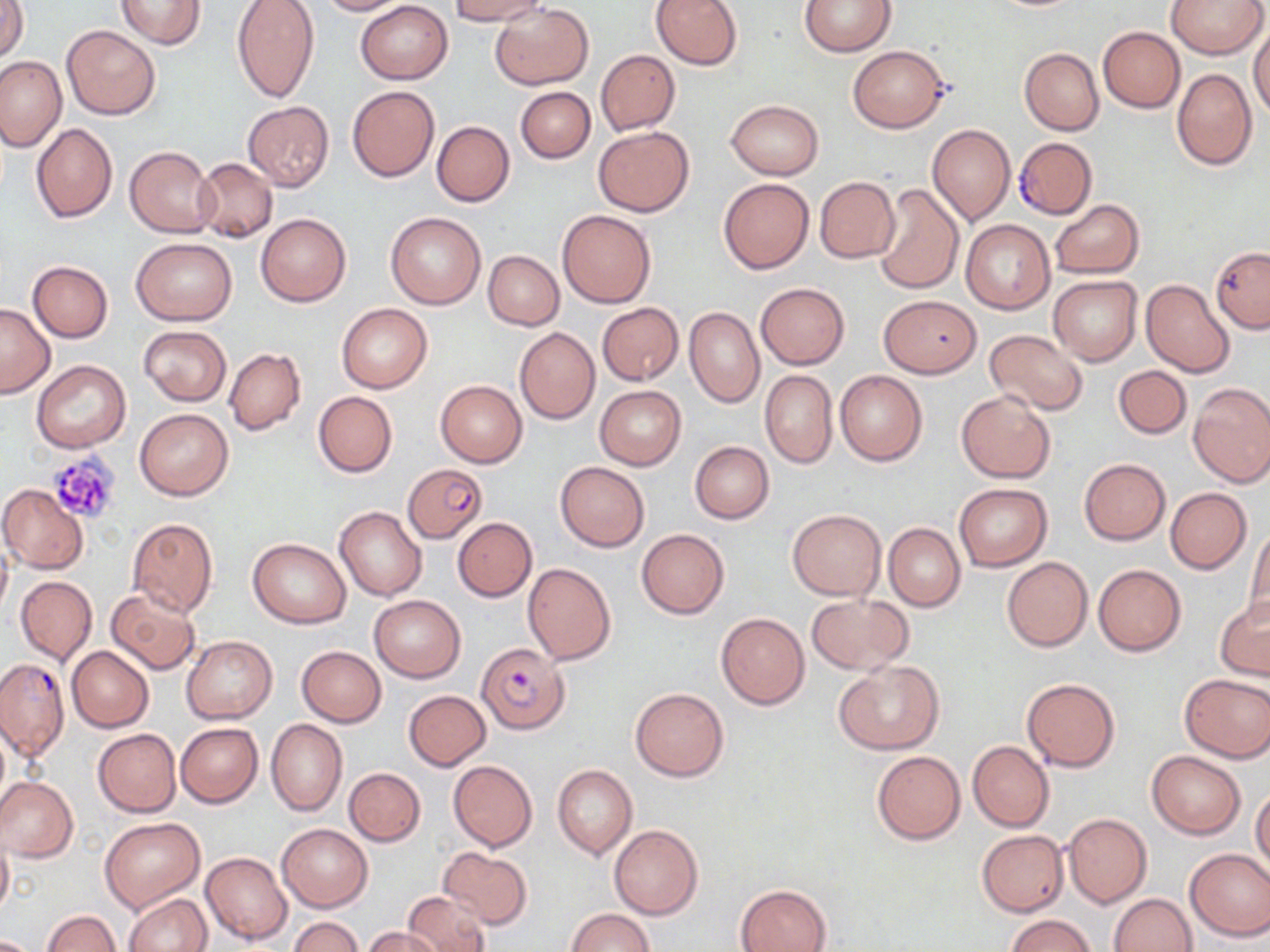

Summary:
  - Coordinate format: approximate bounding boxes as [x1, y1, x2, y2] in pixels
  - Uninfected red blood cell locations: [117, 0, 206, 49], [229, 0, 319, 103], [316, 0, 409, 15], [450, 0, 550, 24], [651, 0, 743, 70], [799, 0, 895, 56], [1166, 0, 1267, 59], [1, 1, 29, 63], [355, 1, 453, 84], [491, 4, 593, 90], [61, 24, 161, 119], [1250, 24, 1270, 122], [1098, 26, 1185, 113], [848, 45, 950, 132], [1019, 48, 1103, 136], [597, 50, 680, 135], [0, 56, 66, 151], [1171, 67, 1257, 170], [347, 85, 439, 182], [515, 86, 595, 163], [726, 100, 822, 179], [243, 101, 334, 191], [431, 120, 515, 207], [30, 123, 117, 223], [927, 124, 1015, 225], [592, 126, 695, 216], [125, 146, 218, 237], [193, 157, 278, 243], [814, 176, 900, 264], [718, 178, 813, 274], [873, 183, 964, 294], [1050, 200, 1143, 278], [557, 209, 656, 308], [386, 211, 486, 309], [256, 213, 351, 306], [960, 219, 1055, 314], [131, 237, 237, 325], [1210, 247, 1270, 332], [483, 250, 564, 330], [27, 261, 112, 343], [1048, 275, 1141, 365], [1141, 279, 1235, 377], [755, 283, 850, 368], [879, 295, 982, 378], [0, 303, 55, 398], [338, 303, 432, 392], [597, 303, 683, 385], [685, 307, 765, 407], [139, 325, 232, 406], [515, 327, 601, 424], [985, 329, 1088, 415], [224, 347, 306, 435], [31, 360, 132, 453], [1114, 365, 1192, 439], [760, 369, 838, 468], [834, 369, 927, 466], [435, 380, 527, 467], [1188, 382, 1270, 487], [594, 385, 686, 470], [956, 390, 1055, 483], [313, 391, 397, 477], [135, 407, 234, 500], [690, 441, 774, 524], [1078, 459, 1169, 545], [555, 462, 649, 551], [954, 483, 1053, 572], [0, 484, 89, 573], [1165, 488, 1252, 574], [334, 505, 427, 600], [787, 508, 886, 600], [126, 518, 218, 617], [452, 518, 536, 601], [884, 523, 965, 611], [1245, 525, 1270, 621], [637, 528, 729, 618], [247, 537, 351, 628], [0, 539, 12, 623], [1002, 556, 1093, 652], [522, 562, 616, 665], [1093, 564, 1186, 656], [16, 576, 98, 665], [106, 589, 201, 676], [369, 594, 466, 683], [806, 594, 912, 675], [1215, 596, 1270, 679], [716, 613, 810, 709], [181, 636, 277, 723], [68, 646, 153, 731], [296, 646, 387, 727], [834, 659, 942, 755], [1179, 673, 1270, 762], [1022, 677, 1120, 772], [630, 687, 728, 781], [404, 690, 490, 770], [266, 718, 347, 816], [176, 723, 263, 807], [92, 728, 180, 817], [967, 741, 1055, 831], [870, 750, 967, 845], [1146, 751, 1245, 839], [448, 760, 537, 851], [553, 765, 637, 859], [344, 767, 426, 846], [0, 777, 79, 863], [1251, 789, 1270, 873], [1062, 812, 1152, 909], [100, 816, 205, 913], [276, 823, 373, 912], [609, 824, 703, 920], [976, 830, 1068, 916], [0, 832, 13, 918], [1185, 847, 1270, 940], [439, 848, 532, 927], [201, 852, 293, 946], [736, 884, 830, 952], [404, 889, 489, 952], [1110, 893, 1196, 952], [124, 894, 211, 952], [566, 909, 653, 952], [42, 910, 120, 952], [1007, 915, 1094, 952], [287, 916, 364, 952], [363, 927, 441, 952]
  - Platelet locations: [46, 451, 122, 525]
  - Plasmodium falciparum-infected red blood cell locations: [1014, 137, 1096, 220], [403, 464, 486, 543], [477, 642, 569, 734], [0, 657, 69, 761]
  - Slide-level diagnosis: Plasmodium falciparum
  - Magnification: 1000x
  - Modality: optical microscopy
  - Image size: 1270×952 pixels
  - Preparation: thin blood smear
  - Stain: May-Grünwald-Giemsa
  - Field of view: one of a larger specimen